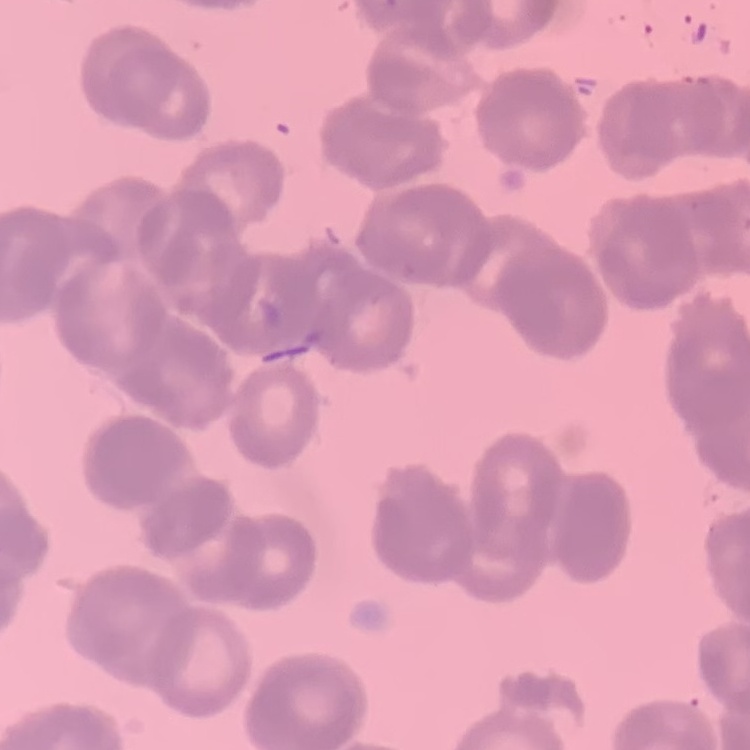 The erythrocytes show rouleaux formation. Field's or Giemsa stain. Square crop of a larger photomicrograph. Thin peripheral smear.